State which parasite is depicted.
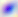
This is Toxoplasma gondii.

Micrograph. Captured at 400x magnification.